Name the parasite shown.
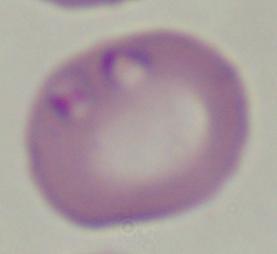

Babesia.

magnification = 1000x
modality = micrograph